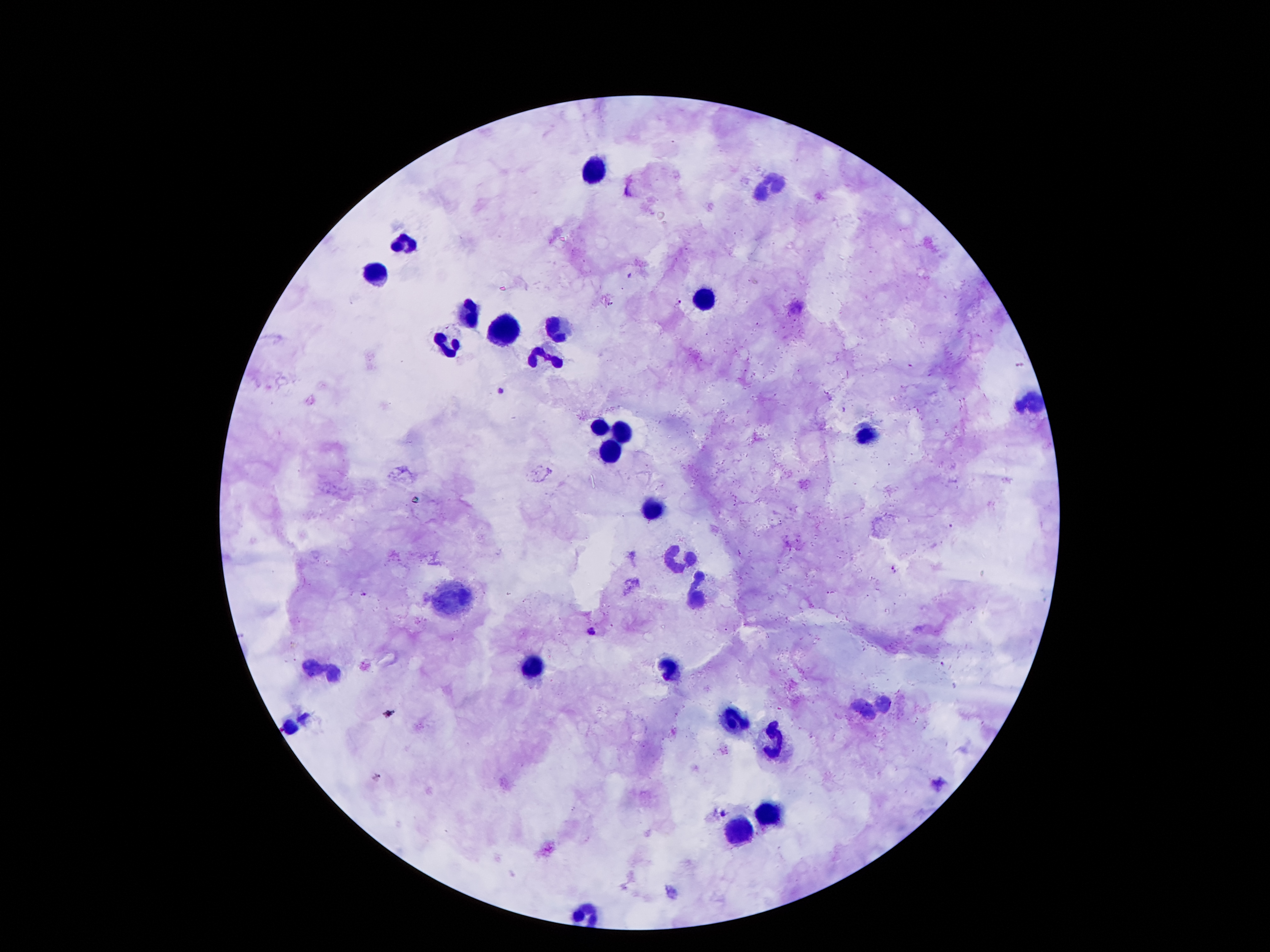

coordinate format = approximate centers as {x, y} in pixels
Plasmodium parasite locations = {679, 300}, {501, 391}, {894, 570}, {365, 594}, {593, 629}, {723, 813}
leukocyte locations = {596, 166}, {770, 185}, {405, 246}, {376, 273}, {706, 300}, {470, 318}, {556, 329}, {506, 337}, {446, 343}, {544, 353}, {1029, 399}, {599, 428}, {622, 429}, {866, 437}, {612, 450}, {657, 509}, {677, 557}, {695, 591}, {452, 597}, {528, 668}, {670, 669}, {328, 673}, {885, 703}, {862, 709}, {730, 722}, {292, 728}, {774, 743}, {770, 812}, {739, 832}
stain = Giemsa
magnification = 100x
image size = 1270×952 pixels
capture = smartphone through the microscope eyepiece
preparation = thick blood film
field of view = single
patient malaria status = positive for Plasmodium falciparum